Name the blood parasite species.
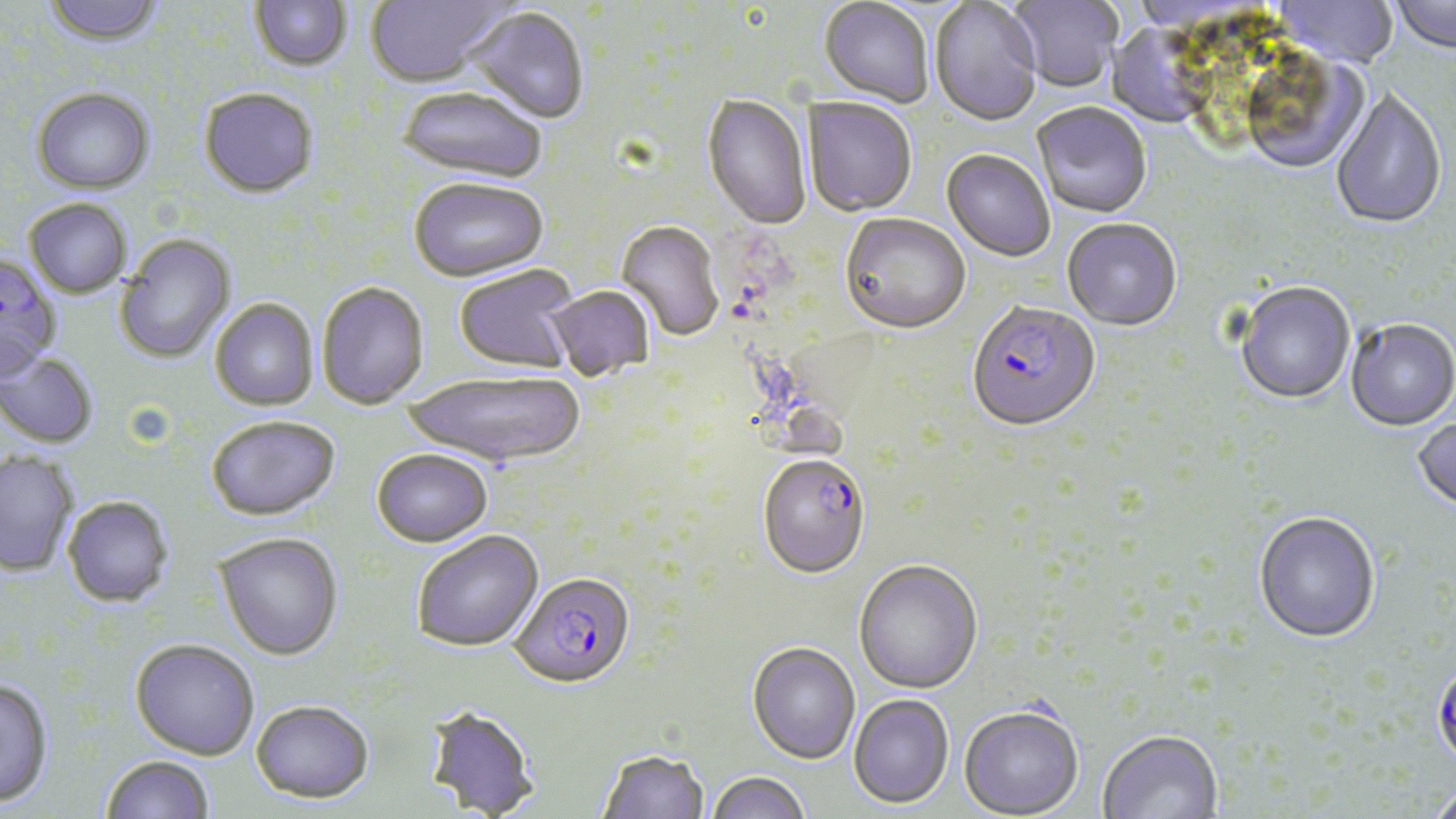
Plasmodium falciparum.

Approximate bounding boxes as (x1,y1)-(x2,y2) corner pairs in pixels. Uninfected red blood cell locations: (41,0)-(166,48), (249,0)-(352,72), (366,0)-(510,90), (1008,0)-(1123,94), (1389,0)-(1456,56), (818,1)-(934,110), (1271,1)-(1399,69), (929,2)-(1043,128), (466,8)-(589,125), (1105,21)-(1218,130), (32,88)-(155,194), (199,88)-(319,198), (397,88)-(546,185), (1331,91)-(1447,232), (701,95)-(812,231), (802,99)-(916,218), (1031,104)-(1152,220), (941,150)-(1055,263), (409,179)-(548,284), (24,198)-(131,297), (839,215)-(971,337), (1062,220)-(1182,333), (616,222)-(724,343), (115,234)-(236,364), (0,253)-(62,383), (455,266)-(579,374), (317,282)-(429,409), (1234,283)-(1355,406), (546,287)-(654,381), (210,299)-(318,411), (1346,320)-(1456,433), (0,351)-(99,449), (405,371)-(586,469), (206,415)-(340,520), (1411,416)-(1456,519), (371,449)-(493,548), (0,451)-(78,577), (63,496)-(174,607), (1253,513)-(1380,644), (413,531)-(544,653), (215,532)-(343,660), (853,560)-(983,695), (130,639)-(259,760), (747,642)-(860,764), (0,678)-(54,808), (848,694)-(954,810), (251,700)-(374,804), (422,705)-(540,818), (959,707)-(1084,818), (1097,730)-(1222,819), (597,750)-(709,819), (101,755)-(215,819), (707,772)-(810,819), (1425,782)-(1456,819). Plasmodium falciparum-infected red blood cell locations: (966,303)-(1101,435), (756,456)-(870,580), (511,574)-(635,692), (1432,661)-(1456,771). May-Grünwald-Giemsa-stained preparation. Single field of view. Image is 1456×819 pixels. Light microscopy. Captured at 1000x magnification. Thin blood film.